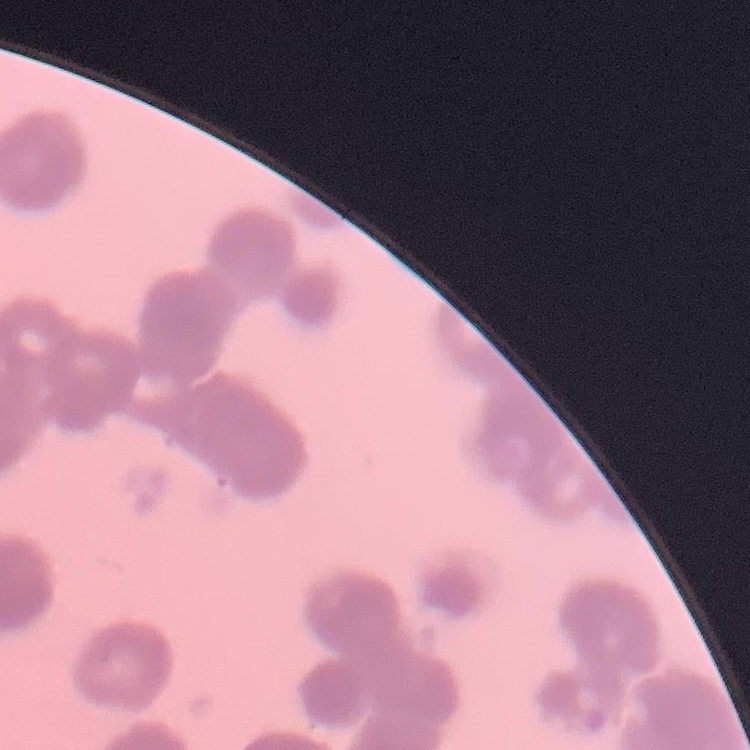
The erythrocytes exhibit rouleaux formation. Thin blood smear. One tile cut from a larger photomicrograph. Stained with either Field's or Giemsa.